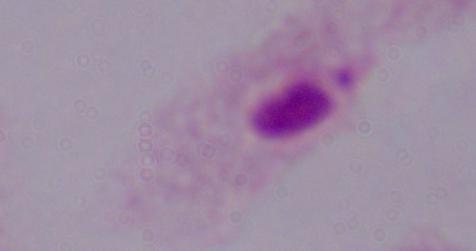
identification: trichomonad
modality: photomicrograph
magnification: 1000x